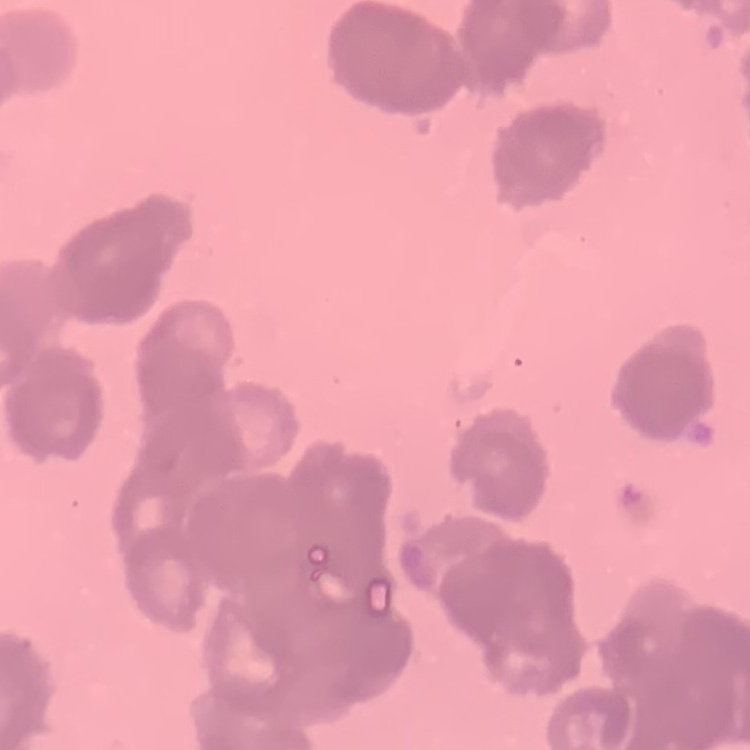

Summary:
  - Erythrocyte morphology: rouleaux formation
  - Preparation: thin blood film
  - Stain: Field's or Giemsa
  - Image type: square crop of a larger photomicrograph